Report the malaria status of this cell.
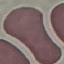
It is uninfected.

Summary:
  - Capture: smartphone through the microscope eyepiece
  - Preparation: thin blood smear
  - Image type: cell patch, automatically extracted from a larger field of view and resized to 64 × 64 pixels
  - Stain: Giemsa